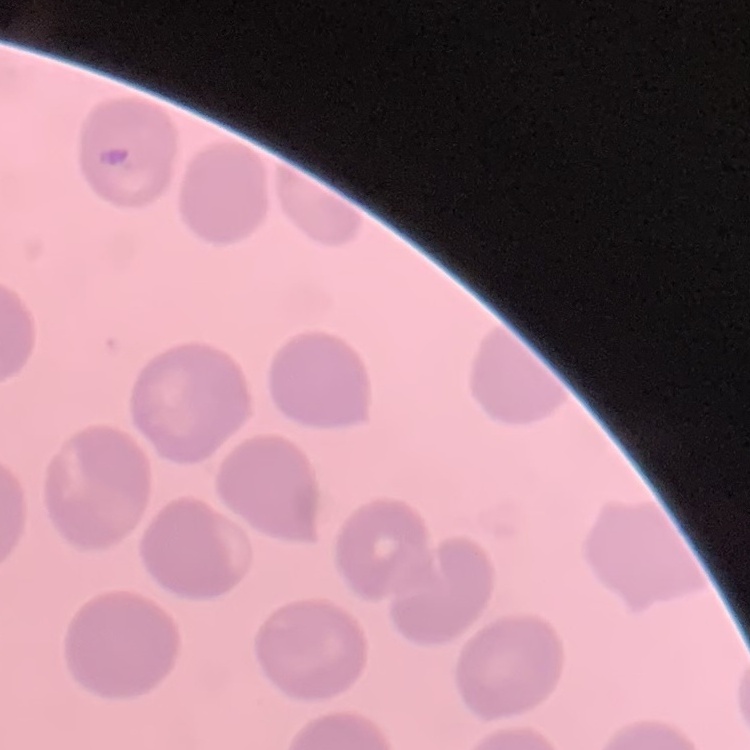

red blood cell morphology = no rouleaux formation
preparation = thin blood film
image type = one tile cut from a larger photomicrograph
stain = Field's or Giemsa